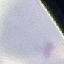
malaria status = uninfected
preparation = thin blood film
capture = smartphone camera at the microscope eyepiece
image type = automatically extracted cell patch, resized to 64 × 64 pixels
stain = Giemsa